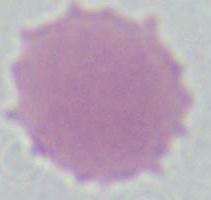
Micrograph. 1000x magnification. A red blood cell is seen.